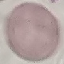

malaria status = uninfected
image type = cell patch, automatically extracted from a larger field of view and resized to 64 × 64 pixels
capture = smartphone camera at the microscope eyepiece
stain = Giemsa
preparation = thin blood smear